Assess this cell for malaria.
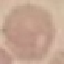

Uninfected.

Giemsa-stained preparation. Automatically extracted cell patch, resized to 64 × 64 pixels. Thin blood smear. Photographed with a smartphone camera at the microscope eyepiece.